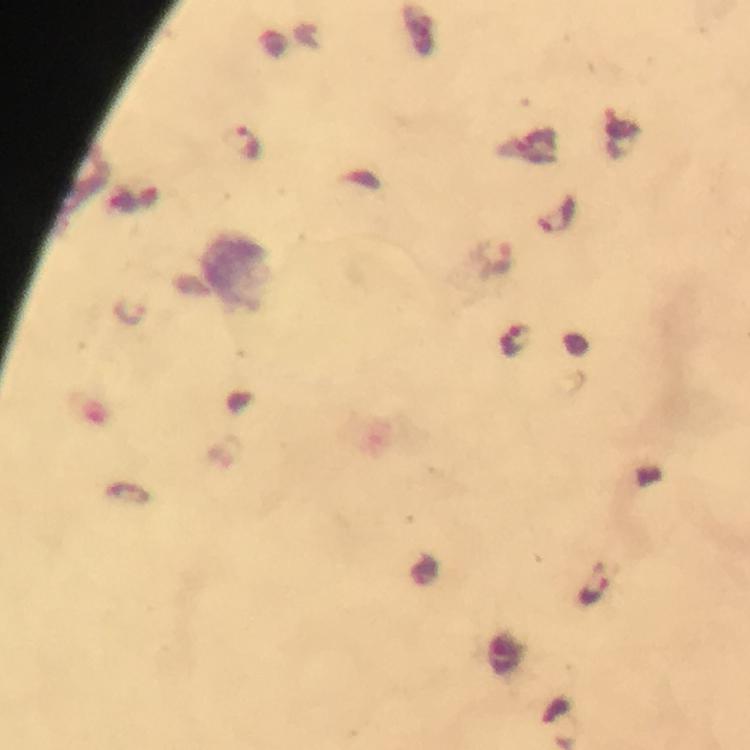

Approximate centers as {x, y} in pixels. Malaria parasite locations: {240, 144}, {494, 257}, {128, 310}, {515, 339}, {594, 590}. Immersion oil applied. Giemsa stain. Image is 750×750 pixels. Thick blood smear. From a diagnostic examination for malaria. Photographed with a smartphone mounted on the microscope. Cropped region of a single field of view. At 100x magnification.